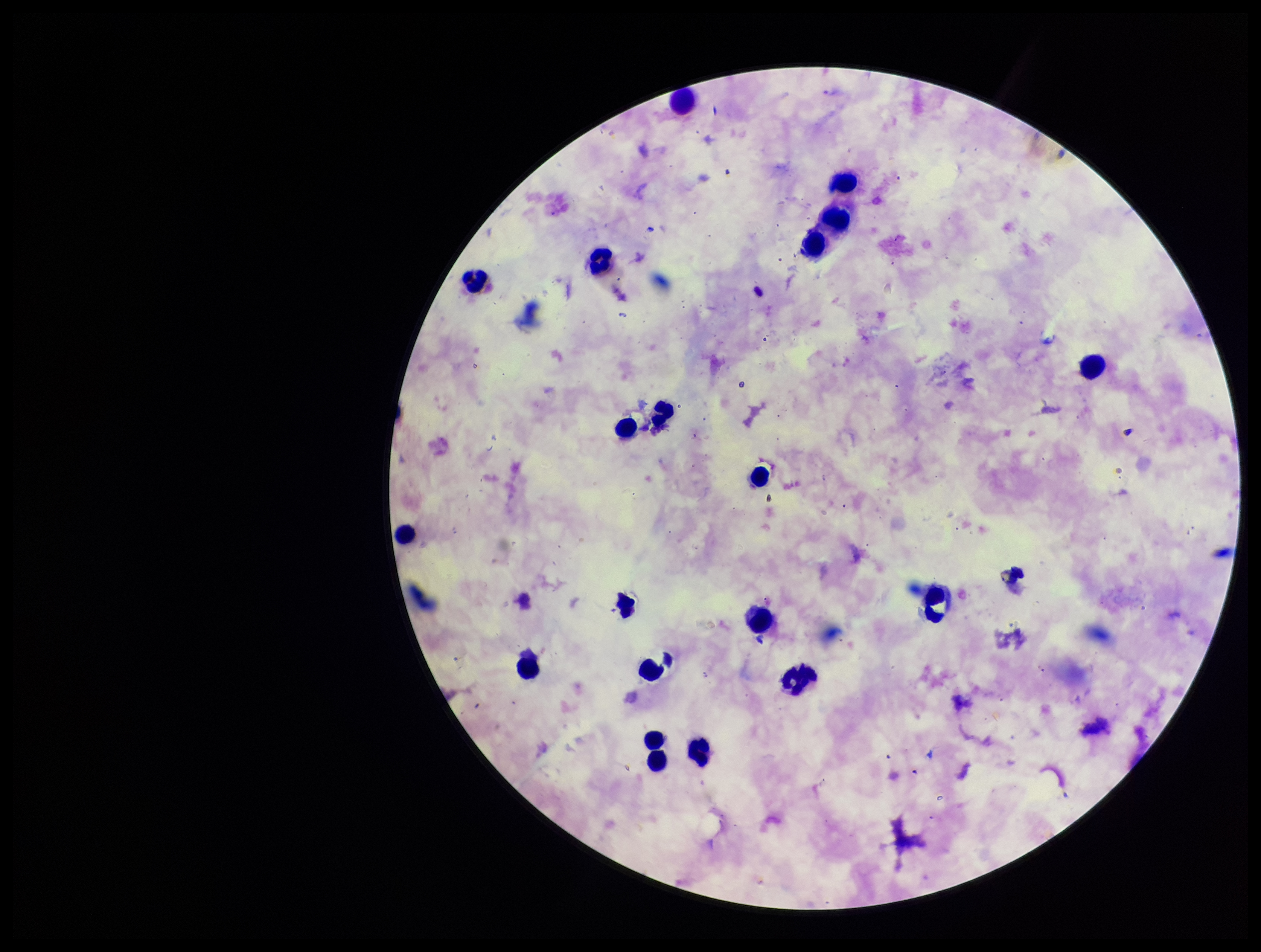
preparation = thick smear
parasite count = 0
leukocyte count = 20
stain = Giemsa
Plasmodium parasites = none identified
image size = 1261×952 pixels
patient malaria status = positive
species reported for this patient = Plasmodium falciparum
capture = smartphone photograph through the microscope eyepiece
field of view = one from this slide